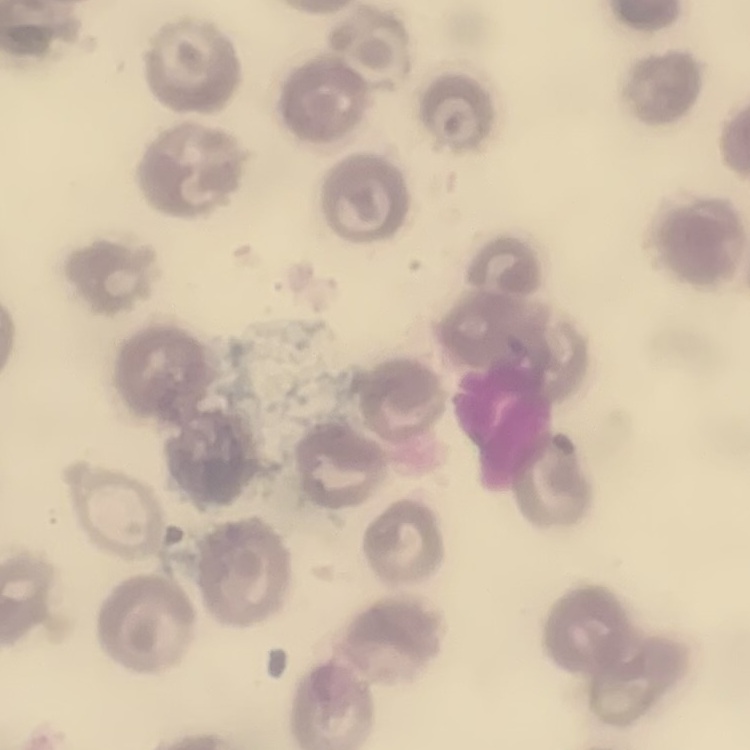
Summary:
  - Red blood cell morphology: no rouleaux formation
  - Stain: Field's or Giemsa
  - Image type: square crop of a larger photomicrograph
  - Preparation: thin blood film